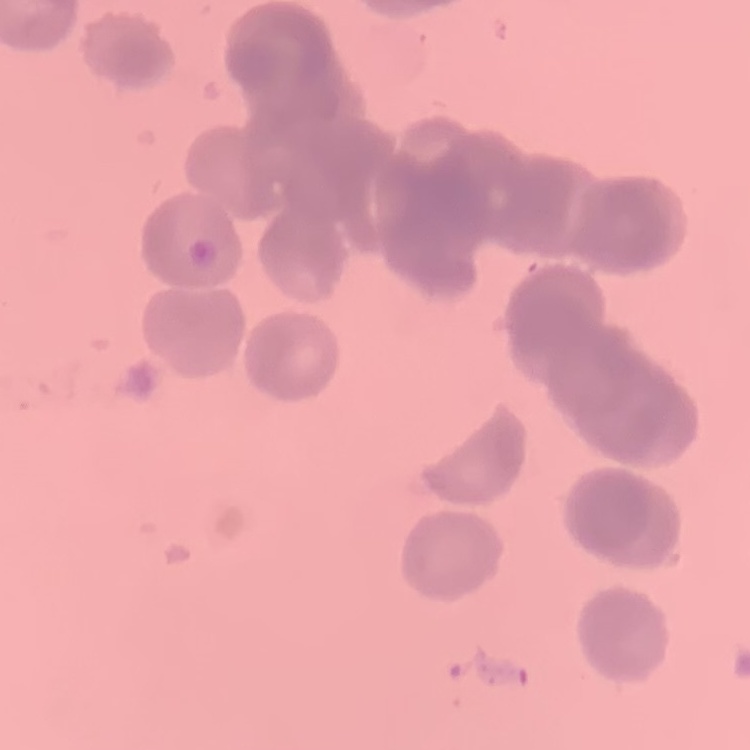

Summary:
  - Red blood cell morphology: rouleaux formation
  - Stain: Field's or Giemsa
  - Image type: one tile cut from a larger photomicrograph
  - Preparation: thin peripheral smear